Report the malaria status of this cell.
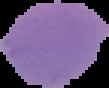

Uninfected.

Summary:
  - Image type: cell region segmented out of the field of view; surrounding area masked to black
  - Image size: 109×88 pixels
  - Preparation: thin blood film